Comment on the morphology of the erythrocytes.
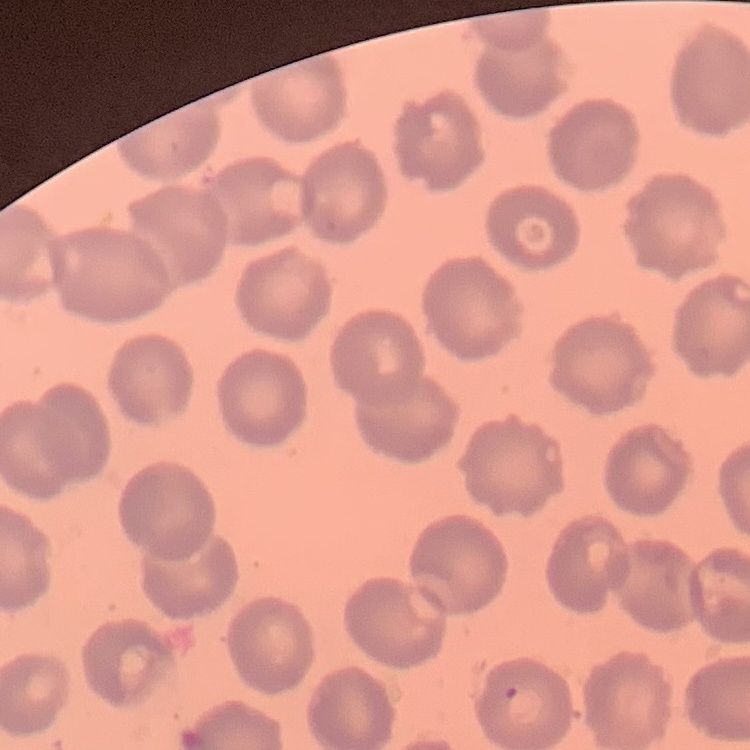

No rouleaux formation.

preparation = thin blood film
image type = one tile cut from a larger photomicrograph
stain = Field's or Giemsa